Classify this cell by malaria status.
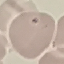
It is uninfected.

image type = cell patch, automatically extracted from a larger field of view and resized to 64 × 64 pixels
capture = smartphone through the microscope eyepiece
stain = Giemsa
preparation = thin blood film